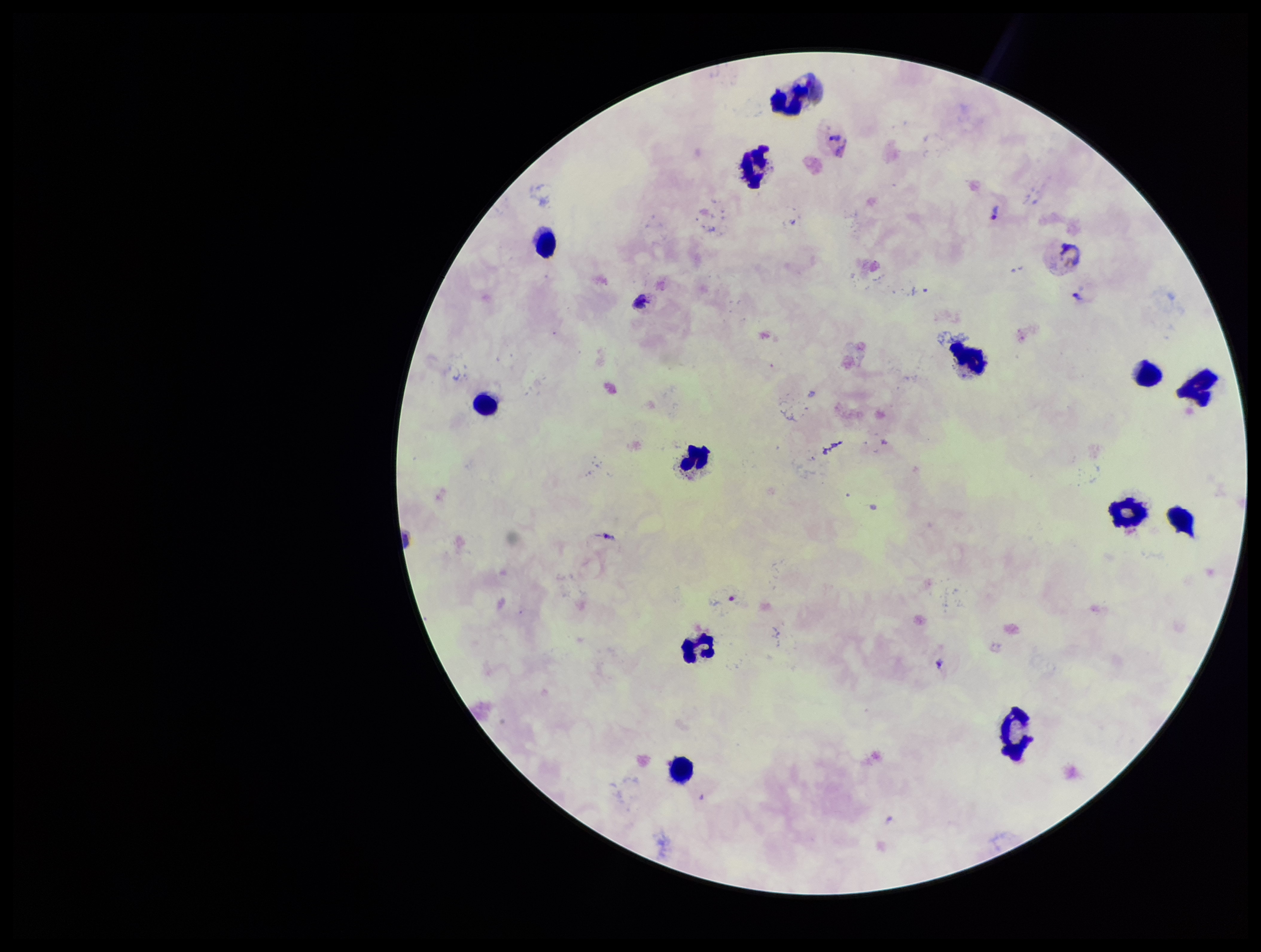

parasite_count: 4
preparation: thick blood smear
field_of_view: single
plasmodium_parasites: seen
leukocyte_count: 13
patient_malaria_status: positive
image_size: 1261×952 pixels
stain: Giemsa
species_reported_for_this_patient: Plasmodium vivax
capture: smartphone photograph through the microscope eyepiece